Name the parasite shown.
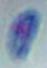

This is Toxoplasma gondii.

Micrograph. Captured at 1000x magnification.